Classify this cell by malaria status.
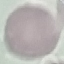
It is uninfected.

{
  "preparation": "thin blood smear",
  "capture": "smartphone camera at the microscope eyepiece",
  "image_type": "cell patch, automatically extracted from a larger field of view and resized to 64 × 64 pixels",
  "stain": "Giemsa"
}